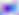
Micrograph. Captured at 400x magnification. Toxoplasma gondii is seen.